Classify the preparation.
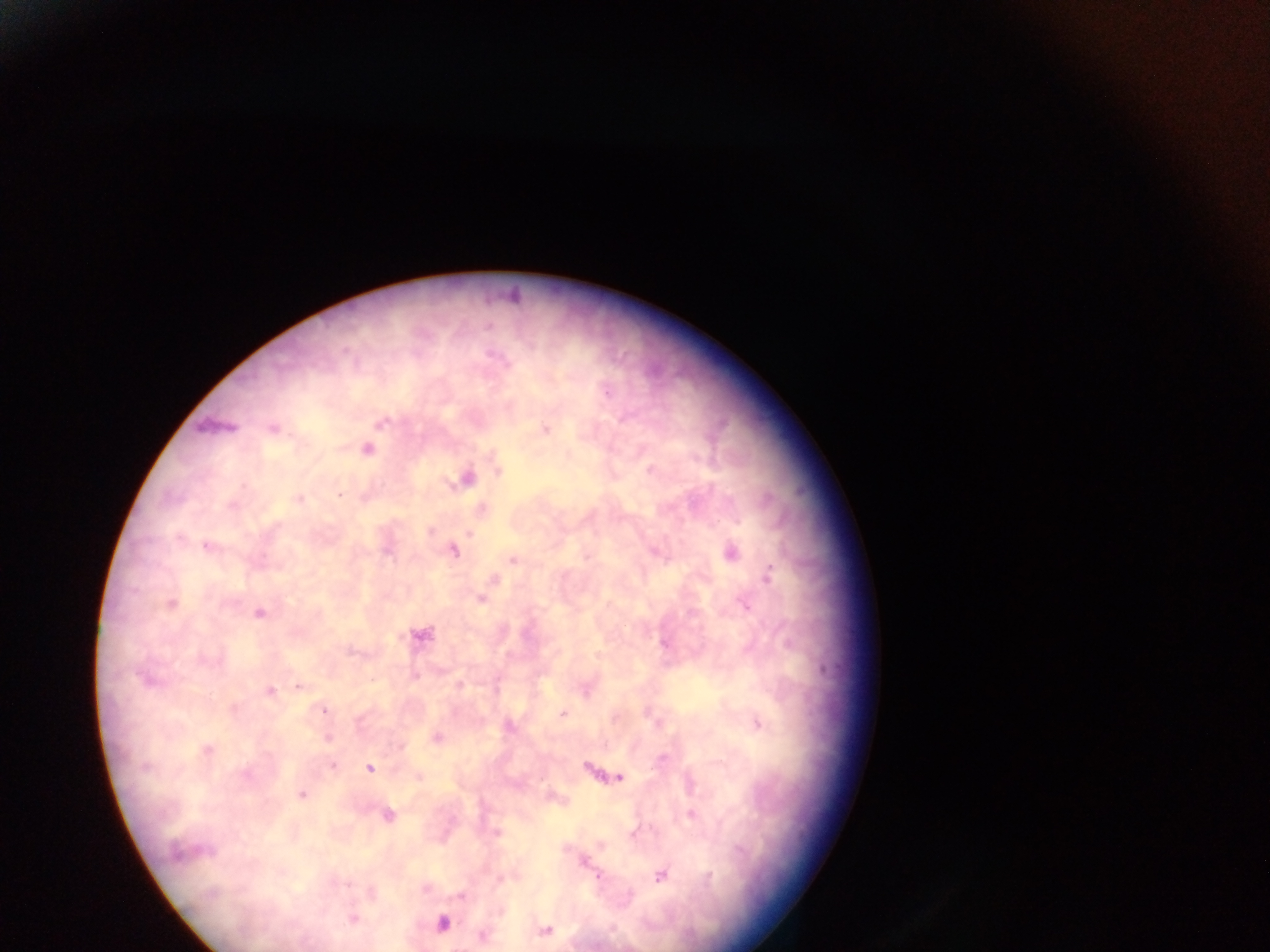

Thick blood smear.

Approximate centers as x y in pixels.
Summary:
  - Malaria parasite locations: 488 326; 607 393; 381 422; 273 429; 545 429; 367 450; 498 470; 651 470; 467 479; 339 493; 298 498; 232 506; 482 509; 431 532; 469 533; 178 539; 207 546; 454 551; 731 553; 587 557; 512 561; 769 575; 494 580; 481 600; 171 604; 746 606; 259 612; 421 636; 664 643; 415 675; 147 679; 460 685; 299 687; 270 691; 233 708; 324 711; 563 714; 758 724; 510 727; 436 737; 327 738; 401 746; 208 750; 661 759; 330 760; 333 766; 145 767; 369 768; 245 775; 418 777; 620 777; 302 795; 691 814; 387 815; 497 833; 634 834; 206 852; 176 853; 584 862; 599 875; 661 876; 710 877; 347 883; 461 897; 352 918; 443 923; 545 930; 482 936
  - Country: Ghana
  - Image size: 1270×952 pixels
  - Field of view: single
  - Capture: mobile-phone photograph through a microscope